State which parasite is depicted.
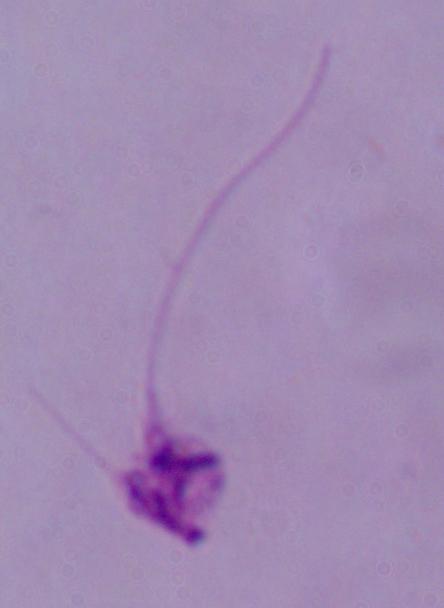

This is Leishmania.

Summary:
  - Magnification: 1000x
  - Modality: micrograph